Outline each Trypanosoma brucei.
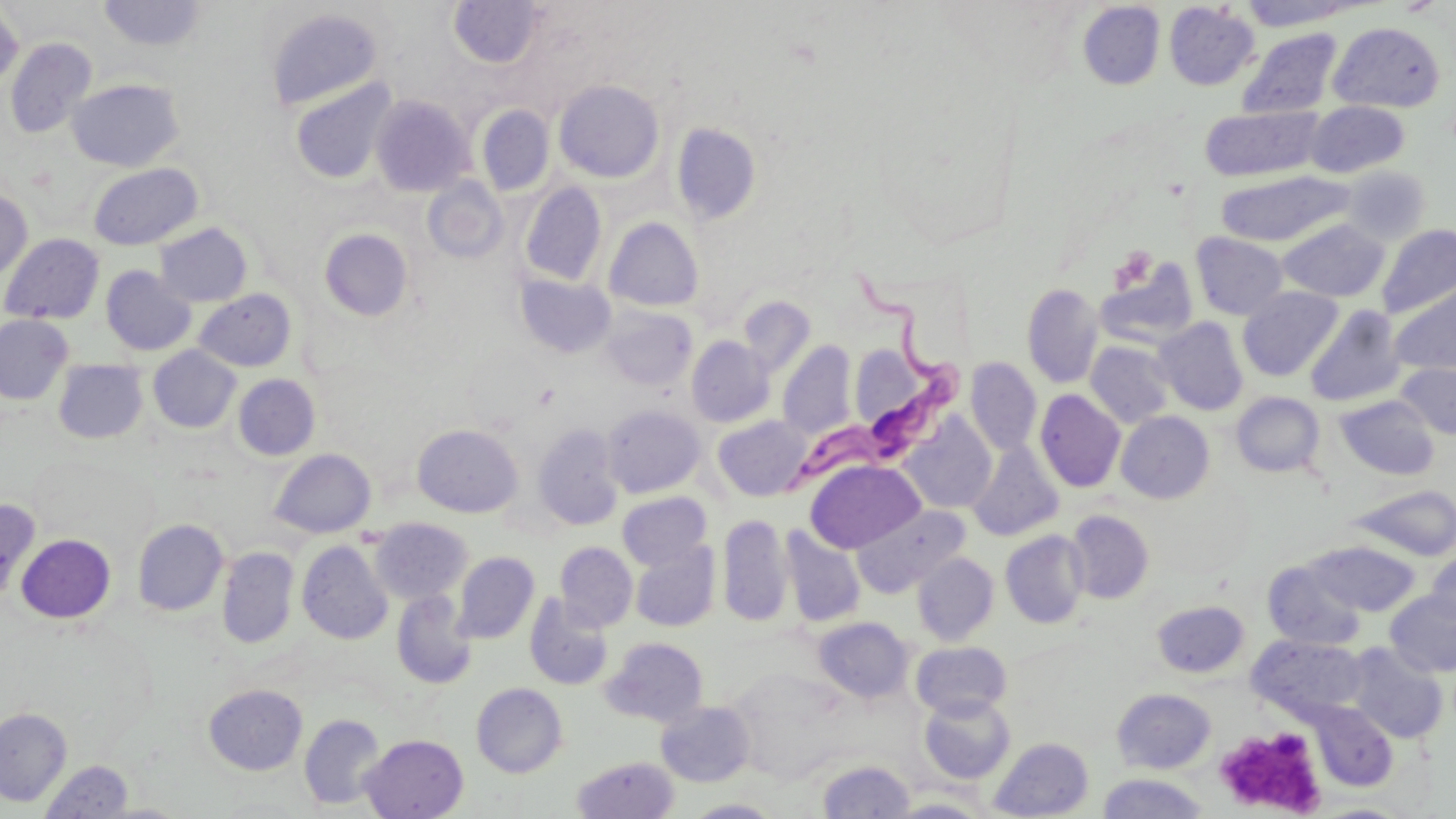

Approximate bounding boxes as (x1, y1, x2, y2) in pixels.
Trypanosoma brucei: (771, 269, 977, 505).

Summary:
  - Platelet locations: (1109, 246, 1158, 294), (1217, 724, 1332, 815)
  - Uninfected red blood cell locations: (97, 1, 210, 53), (449, 1, 544, 69), (1236, 1, 1358, 30), (1077, 2, 1165, 89), (1164, 2, 1259, 90), (264, 6, 384, 112), (0, 7, 24, 92), (1328, 22, 1446, 113), (1236, 27, 1344, 120), (5, 37, 97, 139), (66, 77, 185, 172), (289, 77, 399, 185), (553, 79, 665, 183), (370, 95, 475, 197), (1305, 101, 1409, 178), (1200, 105, 1324, 182), (477, 106, 554, 196), (672, 123, 763, 225), (87, 162, 203, 250), (1341, 165, 1431, 244), (1216, 170, 1352, 247), (423, 176, 509, 262), (519, 180, 607, 287), (0, 187, 32, 282), (604, 216, 704, 312), (1278, 219, 1389, 302), (155, 223, 252, 307), (1377, 224, 1456, 319), (319, 228, 413, 321), (1, 233, 105, 325), (1191, 233, 1289, 320), (1097, 258, 1200, 349), (101, 266, 197, 356), (515, 273, 616, 358), (1388, 280, 1456, 376), (1022, 283, 1103, 388), (1237, 286, 1343, 381), (193, 289, 296, 371), (737, 296, 815, 378), (600, 305, 697, 390), (1304, 305, 1406, 408), (0, 314, 73, 405), (1154, 317, 1248, 416), (687, 336, 774, 427), (1085, 340, 1174, 428), (778, 341, 856, 439), (848, 343, 933, 438), (148, 346, 241, 433), (966, 357, 1042, 455), (53, 359, 148, 444), (1397, 363, 1456, 439), (234, 373, 320, 460), (1035, 389, 1126, 493), (1231, 392, 1325, 477), (1335, 395, 1440, 480), (602, 404, 705, 497), (1116, 411, 1214, 503), (900, 413, 997, 514), (713, 415, 812, 501), (532, 423, 624, 530), (412, 424, 522, 517), (967, 441, 1063, 541), (270, 448, 376, 539), (805, 459, 925, 552), (1351, 484, 1456, 560), (617, 492, 711, 570), (851, 503, 970, 596), (1066, 510, 1154, 603), (718, 514, 792, 627), (371, 517, 472, 604), (133, 519, 228, 616), (781, 528, 865, 627), (1001, 530, 1090, 628), (16, 533, 115, 623), (297, 541, 393, 643), (1310, 541, 1419, 615), (554, 542, 638, 631), (630, 542, 719, 632), (217, 547, 298, 648), (453, 551, 539, 643), (912, 552, 999, 646), (1425, 552, 1456, 629), (1264, 559, 1365, 650), (1385, 589, 1456, 677), (392, 590, 476, 688), (524, 595, 613, 690), (1152, 600, 1249, 677), (813, 616, 913, 703), (1247, 634, 1366, 721), (602, 637, 708, 726), (911, 640, 1011, 719), (1347, 643, 1448, 743), (471, 682, 568, 777), (203, 684, 307, 775), (1112, 688, 1216, 773), (919, 694, 1015, 783), (656, 700, 755, 786), (1311, 702, 1397, 791), (1, 707, 72, 806), (299, 713, 386, 810), (360, 734, 468, 818), (989, 736, 1094, 818), (572, 756, 679, 818), (40, 759, 133, 818), (816, 759, 915, 818), (1095, 773, 1211, 819), (884, 797, 993, 818), (685, 798, 782, 818)
  - Slide-level diagnosis: Trypanosoma brucei
  - Modality: light microscopy
  - Field of view: one of a larger specimen
  - Image size: 1456×819 pixels
  - Stain: May-Grünwald-Giemsa
  - Preparation: thin blood smear
  - Magnification: 1000x